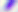
{
  "identification": "Toxoplasma gondii",
  "magnification": "400x",
  "modality": "micrograph"
}